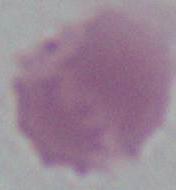

Summary:
  - Identification: erythrocyte
  - Magnification: 1000x
  - Modality: micrograph